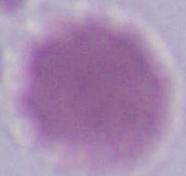
A red blood cell is seen. 1000x magnification. Micrograph.